Assess this cell for malaria.
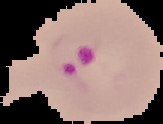

Parasitized.

From a thin blood film. Cell region segmented out of the field of view; the surrounding area is masked to black. Image is 163×124 pixels.